Give the extent of all Plasmodium falciparum-infected red blood cells.
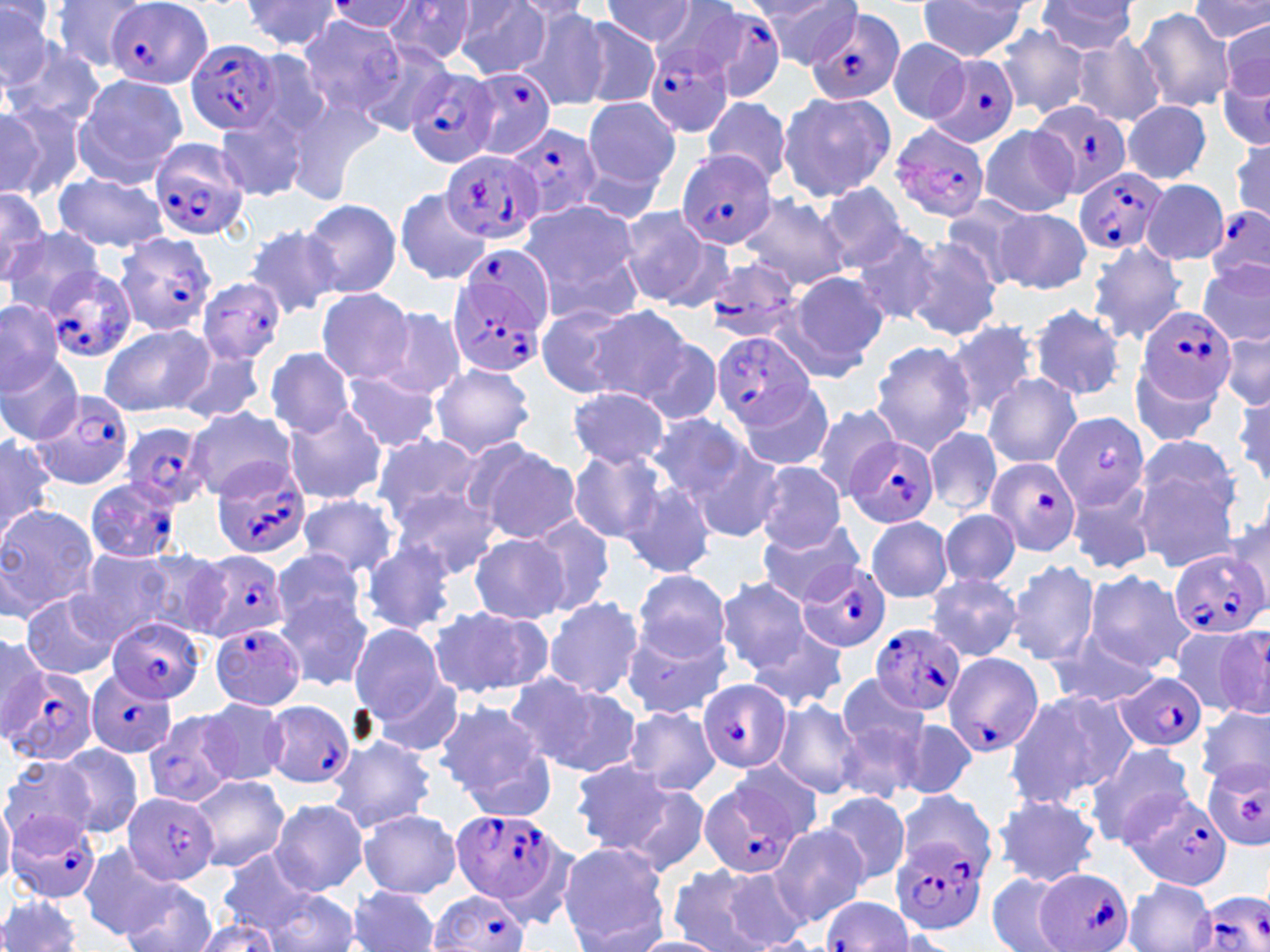

Approximate bounding boxes as (x1, y1, x2, y2) in pixels.
Plasmodium falciparum-infected red blood cells (subset): (103, 1, 213, 88), (684, 5, 787, 104), (805, 8, 905, 106), (186, 38, 281, 136), (645, 41, 737, 138), (929, 52, 1021, 149), (467, 66, 556, 161), (405, 67, 499, 169), (1033, 100, 1132, 201), (502, 123, 600, 220), (889, 124, 991, 223), (149, 138, 251, 242), (440, 148, 547, 245), (676, 150, 775, 249), (1075, 167, 1167, 257), (1205, 205, 1270, 287), (114, 231, 217, 337), (450, 251, 549, 376), (699, 260, 810, 343), (41, 268, 139, 365), (1137, 304, 1236, 405), (711, 332, 815, 429), (27, 386, 137, 495), (1050, 411, 1149, 513), (122, 421, 213, 511), (845, 435, 939, 530), (985, 458, 1080, 557), (211, 463, 311, 561), (84, 478, 184, 564), (1168, 547, 1266, 640), (186, 550, 290, 643), (797, 561, 891, 653), (107, 619, 202, 703), (211, 622, 308, 711), (871, 624, 964, 716), (942, 651, 1043, 758), (3, 666, 100, 768), (86, 669, 178, 760), (1115, 672, 1209, 752), (696, 679, 791, 772), (261, 699, 357, 789), (1204, 759, 1268, 852), (699, 775, 808, 880), (1124, 791, 1232, 891), (448, 807, 569, 910), (5, 813, 104, 905), (891, 836, 992, 935), (1037, 867, 1135, 952), (429, 892, 531, 952), (1195, 892, 1270, 952), (823, 895, 913, 951).

Summary:
  - Uninfected red blood cell locations (subset): (50, 0, 152, 73), (600, 0, 700, 47), (755, 0, 864, 70), (916, 0, 1032, 60), (1192, 0, 1270, 44), (1, 1, 58, 89), (239, 1, 346, 52), (325, 1, 419, 33), (455, 1, 550, 77), (383, 2, 480, 65), (648, 2, 747, 79), (1034, 2, 1139, 53), (518, 6, 608, 111), (1136, 8, 1236, 111), (1220, 17, 1270, 105), (295, 18, 411, 118), (578, 19, 660, 109), (993, 23, 1089, 119), (1071, 35, 1165, 128), (5, 38, 102, 129), (886, 38, 973, 125), (355, 40, 456, 138), (1217, 50, 1269, 156), (73, 74, 188, 183), (776, 91, 895, 203), (283, 92, 387, 204), (702, 95, 792, 187), (581, 97, 680, 194), (0, 98, 81, 201), (1122, 101, 1211, 183), (0, 106, 41, 195), (213, 113, 306, 201), (977, 125, 1078, 217), (1229, 135, 1269, 226), (55, 172, 167, 250), (1144, 180, 1229, 266), (817, 184, 915, 270), (0, 187, 51, 281), (394, 188, 490, 284), (738, 192, 851, 291), (943, 198, 1035, 289), (301, 199, 402, 298), (517, 200, 641, 308), (613, 207, 719, 306), (994, 209, 1091, 293), (242, 224, 342, 318), (6, 226, 104, 313), (850, 231, 943, 324), (897, 236, 1004, 341), (1085, 241, 1188, 345), (1200, 261, 1269, 346), (785, 271, 891, 372), (316, 288, 415, 384), (0, 298, 66, 393), (534, 304, 645, 398), (1029, 305, 1127, 402), (583, 306, 694, 403), (379, 307, 468, 399), (947, 320, 1042, 418), (100, 322, 213, 418), (1221, 329, 1269, 409), (638, 338, 723, 426), (868, 340, 979, 455), (264, 347, 355, 436), (173, 351, 268, 423), (0, 355, 84, 445), (1130, 362, 1224, 450), (428, 363, 535, 458), (339, 373, 444, 452), (982, 374, 1080, 470), (742, 382, 833, 470), (1232, 384, 1270, 488), (567, 387, 669, 467), (806, 401, 902, 500), (283, 406, 386, 505), (185, 408, 296, 499), (648, 412, 755, 503), (925, 427, 1002, 516), (0, 434, 55, 543), (369, 435, 484, 526), (1135, 435, 1240, 523), (686, 439, 788, 544), (468, 440, 581, 544), (368, 447, 486, 612), (568, 448, 671, 543), (1131, 457, 1244, 574), (752, 460, 847, 551), (620, 478, 718, 580), (1064, 481, 1156, 577), (389, 484, 503, 580), (297, 493, 402, 577), (0, 504, 98, 623), (940, 509, 1021, 587), (526, 516, 615, 616), (865, 517, 952, 602), (755, 519, 868, 605), (467, 534, 569, 624), (360, 541, 458, 636), (72, 546, 179, 644), (272, 546, 368, 635), (130, 550, 227, 636), (1007, 559, 1101, 665), (631, 569, 731, 661), (1082, 569, 1195, 674), (926, 573, 1021, 659), (715, 577, 821, 679), (19, 590, 123, 680), (275, 591, 375, 693), (542, 596, 643, 699), (427, 605, 553, 700), (349, 624, 451, 725), (1181, 624, 1269, 718), (620, 625, 730, 718), (747, 628, 849, 713), (0, 634, 49, 737), (1046, 637, 1159, 708), (835, 672, 928, 760), (509, 674, 642, 777), (373, 677, 465, 756), (1004, 688, 1136, 808), (197, 698, 289, 786), (771, 698, 863, 797), (434, 700, 549, 800), (623, 704, 720, 797), (1198, 704, 1270, 789), (142, 707, 239, 807), (605, 710, 715, 865), (889, 715, 977, 800), (834, 719, 923, 806), (326, 732, 436, 834), (454, 737, 560, 823), (1082, 742, 1197, 848), (55, 744, 144, 838), (0, 756, 99, 848), (569, 757, 676, 853), (189, 776, 288, 873), (622, 781, 711, 875), (821, 791, 913, 888), (896, 791, 997, 876), (993, 792, 1101, 886), (0, 797, 14, 888), (269, 797, 370, 896), (358, 809, 461, 897), (768, 824, 866, 927), (557, 841, 670, 948), (79, 842, 181, 940), (214, 853, 326, 938), (666, 864, 785, 952), (716, 867, 811, 951), (986, 871, 1079, 952), (118, 878, 217, 952), (1125, 878, 1215, 951), (346, 887, 441, 952), (263, 889, 360, 952), (0, 895, 85, 952), (189, 917, 285, 952), (628, 936, 732, 952)
  - Slide-level diagnosis: Plasmodium falciparum
  - Modality: light microscopy
  - Preparation: thin blood film
  - Field of view: single
  - Image size: 1270×952 pixels
  - Magnification: 1000x
  - Stain: May-Grünwald-Giemsa